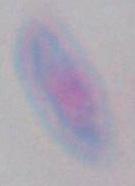

{
  "identification": "Toxoplasma gondii",
  "magnification": "1000x",
  "modality": "photomicrograph"
}